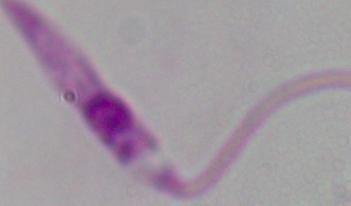

magnification = 1000x
modality = micrograph
identification = Leishmania